Outline each uninfected red blood cell.
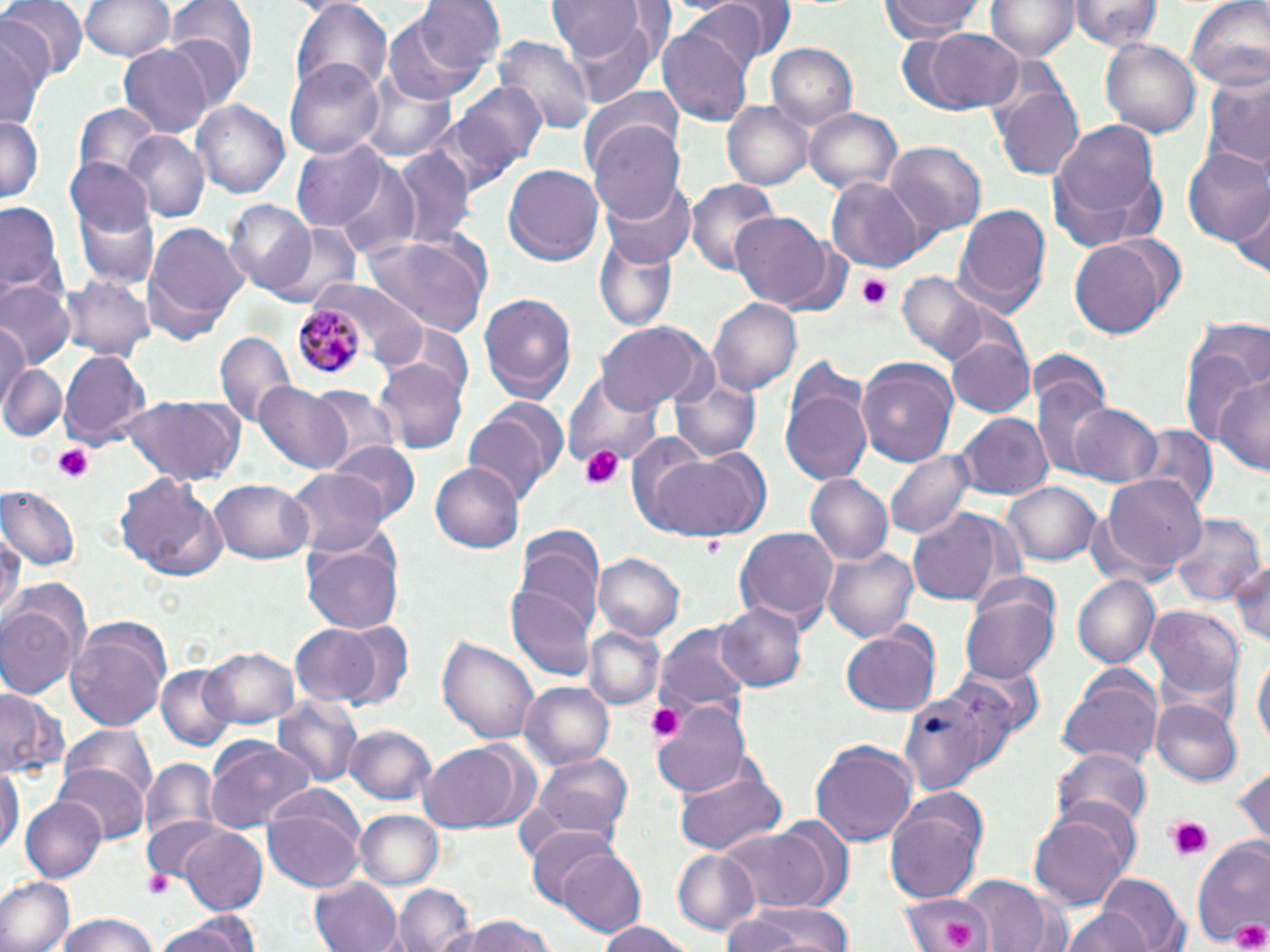
Approximate bounding boxes as named x1/y1/x2/y2 corners in pixels.
Uninfected red blood cells: (x1=1, y1=0, x2=84, y2=81), (x1=79, y1=0, x2=174, y2=63), (x1=165, y1=0, x2=258, y2=84), (x1=291, y1=0, x2=392, y2=99), (x1=411, y1=0, x2=506, y2=79), (x1=881, y1=0, x2=983, y2=43), (x1=988, y1=0, x2=1078, y2=63), (x1=1073, y1=0, x2=1160, y2=50), (x1=1186, y1=0, x2=1270, y2=94), (x1=676, y1=1, x2=772, y2=77), (x1=548, y1=2, x2=646, y2=61), (x1=380, y1=9, x2=493, y2=106), (x1=566, y1=16, x2=659, y2=108), (x1=659, y1=23, x2=755, y2=129), (x1=0, y1=25, x2=46, y2=133), (x1=911, y1=29, x2=1026, y2=115), (x1=496, y1=33, x2=596, y2=136), (x1=1101, y1=38, x2=1200, y2=140), (x1=118, y1=44, x2=213, y2=138), (x1=768, y1=44, x2=856, y2=132), (x1=285, y1=60, x2=384, y2=160), (x1=1200, y1=73, x2=1270, y2=171), (x1=360, y1=76, x2=458, y2=164), (x1=451, y1=81, x2=548, y2=179), (x1=994, y1=84, x2=1084, y2=182), (x1=579, y1=87, x2=686, y2=182), (x1=195, y1=101, x2=288, y2=200), (x1=723, y1=102, x2=812, y2=190), (x1=72, y1=103, x2=164, y2=190), (x1=804, y1=107, x2=902, y2=196), (x1=0, y1=113, x2=43, y2=205), (x1=1047, y1=116, x2=1167, y2=244), (x1=588, y1=121, x2=685, y2=224), (x1=122, y1=133, x2=208, y2=223), (x1=291, y1=140, x2=391, y2=230), (x1=882, y1=141, x2=987, y2=237), (x1=1184, y1=148, x2=1270, y2=246), (x1=393, y1=150, x2=476, y2=247), (x1=66, y1=156, x2=155, y2=240), (x1=332, y1=164, x2=426, y2=260), (x1=503, y1=164, x2=604, y2=265), (x1=826, y1=178, x2=927, y2=271), (x1=687, y1=179, x2=783, y2=275), (x1=604, y1=182, x2=694, y2=265), (x1=1232, y1=190, x2=1270, y2=279), (x1=0, y1=195, x2=67, y2=310), (x1=227, y1=201, x2=318, y2=297), (x1=74, y1=202, x2=159, y2=291), (x1=953, y1=202, x2=1052, y2=319), (x1=732, y1=213, x2=833, y2=309), (x1=268, y1=219, x2=365, y2=310), (x1=142, y1=222, x2=247, y2=343), (x1=593, y1=232, x2=680, y2=333), (x1=360, y1=233, x2=491, y2=334), (x1=1069, y1=235, x2=1181, y2=341), (x1=897, y1=273, x2=987, y2=361), (x1=62, y1=274, x2=155, y2=360), (x1=1, y1=281, x2=74, y2=367), (x1=323, y1=282, x2=431, y2=368), (x1=479, y1=294, x2=577, y2=403), (x1=708, y1=296, x2=801, y2=396), (x1=1180, y1=319, x2=1269, y2=457), (x1=597, y1=322, x2=710, y2=412), (x1=0, y1=326, x2=30, y2=406), (x1=215, y1=330, x2=294, y2=428), (x1=947, y1=335, x2=1036, y2=420), (x1=58, y1=349, x2=150, y2=449), (x1=856, y1=356, x2=959, y2=465), (x1=374, y1=359, x2=468, y2=456), (x1=780, y1=359, x2=876, y2=489), (x1=0, y1=364, x2=67, y2=444), (x1=1217, y1=369, x2=1270, y2=476), (x1=1033, y1=371, x2=1114, y2=477), (x1=565, y1=372, x2=663, y2=472), (x1=671, y1=375, x2=760, y2=461), (x1=253, y1=381, x2=353, y2=474), (x1=304, y1=385, x2=398, y2=469), (x1=118, y1=396, x2=244, y2=484), (x1=1070, y1=402, x2=1162, y2=488), (x1=464, y1=404, x2=562, y2=506), (x1=956, y1=415, x2=1052, y2=499), (x1=1128, y1=424, x2=1218, y2=516), (x1=328, y1=441, x2=420, y2=527), (x1=886, y1=445, x2=975, y2=539), (x1=640, y1=446, x2=772, y2=542), (x1=430, y1=461, x2=525, y2=554), (x1=286, y1=471, x2=388, y2=555), (x1=1099, y1=471, x2=1203, y2=576), (x1=804, y1=473, x2=894, y2=566), (x1=115, y1=475, x2=227, y2=580), (x1=210, y1=479, x2=313, y2=564), (x1=1003, y1=480, x2=1102, y2=563), (x1=2, y1=485, x2=81, y2=566), (x1=907, y1=510, x2=1010, y2=607), (x1=1169, y1=512, x2=1263, y2=606), (x1=734, y1=524, x2=840, y2=632), (x1=513, y1=527, x2=604, y2=634), (x1=0, y1=528, x2=21, y2=628), (x1=301, y1=529, x2=405, y2=636), (x1=825, y1=544, x2=921, y2=643), (x1=594, y1=553, x2=684, y2=640), (x1=1228, y1=553, x2=1270, y2=648), (x1=1074, y1=576, x2=1159, y2=669), (x1=505, y1=584, x2=595, y2=682), (x1=961, y1=592, x2=1058, y2=683), (x1=0, y1=595, x2=82, y2=699), (x1=717, y1=601, x2=806, y2=692), (x1=1146, y1=604, x2=1245, y2=704), (x1=330, y1=619, x2=415, y2=712), (x1=653, y1=621, x2=755, y2=721), (x1=290, y1=623, x2=387, y2=706), (x1=64, y1=624, x2=170, y2=733), (x1=583, y1=625, x2=666, y2=711), (x1=841, y1=628, x2=941, y2=716), (x1=438, y1=634, x2=539, y2=746), (x1=201, y1=644, x2=300, y2=729), (x1=1251, y1=653, x2=1268, y2=756), (x1=154, y1=664, x2=239, y2=750), (x1=1057, y1=668, x2=1163, y2=771), (x1=519, y1=681, x2=614, y2=770), (x1=894, y1=681, x2=1011, y2=793), (x1=0, y1=689, x2=67, y2=782), (x1=275, y1=695, x2=366, y2=791), (x1=652, y1=696, x2=753, y2=799), (x1=1153, y1=700, x2=1242, y2=787), (x1=57, y1=724, x2=159, y2=815), (x1=345, y1=726, x2=435, y2=806), (x1=204, y1=735, x2=318, y2=829), (x1=810, y1=738, x2=918, y2=846), (x1=417, y1=740, x2=535, y2=834), (x1=1055, y1=748, x2=1153, y2=831), (x1=527, y1=753, x2=634, y2=845), (x1=140, y1=756, x2=219, y2=850), (x1=1233, y1=760, x2=1270, y2=848), (x1=0, y1=761, x2=22, y2=856), (x1=56, y1=762, x2=149, y2=847), (x1=674, y1=766, x2=787, y2=857), (x1=885, y1=792, x2=988, y2=901), (x1=21, y1=797, x2=105, y2=882), (x1=261, y1=808, x2=364, y2=894), (x1=357, y1=810, x2=444, y2=891), (x1=1029, y1=810, x2=1133, y2=910), (x1=141, y1=815, x2=236, y2=892), (x1=716, y1=824, x2=844, y2=910), (x1=178, y1=826, x2=269, y2=913), (x1=525, y1=827, x2=625, y2=911), (x1=1192, y1=837, x2=1270, y2=951), (x1=546, y1=843, x2=647, y2=935), (x1=671, y1=850, x2=760, y2=937), (x1=1095, y1=872, x2=1187, y2=952), (x1=960, y1=874, x2=1061, y2=952), (x1=312, y1=875, x2=402, y2=952), (x1=1, y1=876, x2=76, y2=952), (x1=395, y1=883, x2=474, y2=952), (x1=900, y1=890, x2=993, y2=952), (x1=722, y1=901, x2=853, y2=952), (x1=1060, y1=909, x2=1152, y2=952), (x1=156, y1=910, x2=259, y2=952), (x1=50, y1=912, x2=163, y2=952), (x1=438, y1=915, x2=566, y2=952), (x1=594, y1=921, x2=695, y2=952).

slide-level diagnosis = Plasmodium malariae
image size = 1270×952 pixels
preparation = thin blood film
magnification = 1000x
modality = optical microscopy
stain = May-Grünwald-Giemsa
platelet locations = approximate bounding boxes as named x1/y1/x2/y2 corners in pixels: (x1=858, y1=274, x2=894, y2=311), (x1=51, y1=444, x2=97, y2=485), (x1=581, y1=446, x2=626, y2=491), (x1=645, y1=700, x2=687, y2=744), (x1=1165, y1=818, x2=1213, y2=860), (x1=146, y1=869, x2=172, y2=901), (x1=943, y1=919, x2=975, y2=948), (x1=1230, y1=919, x2=1270, y2=952)
field of view = single
Plasmodium malariae-infected red blood cell locations = approximate bounding boxes as named x1/y1/x2/y2 corners in pixels: (x1=294, y1=301, x2=364, y2=380)